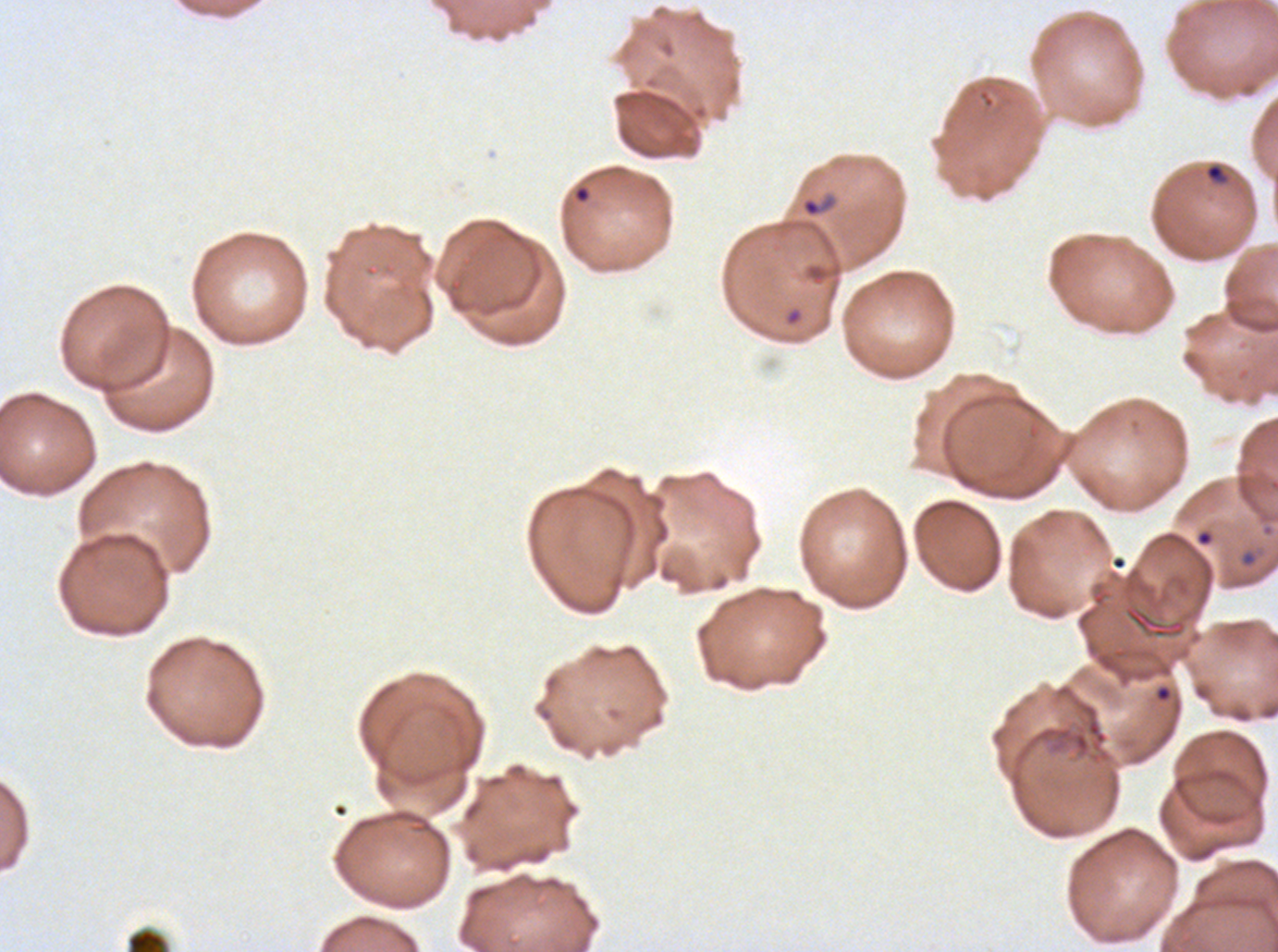

Approximate bounding boxes as [x1, y1, x2, y2] in pixels. Debris locations: [1026, 701, 1111, 764], [126, 927, 169, 951]. Ring locations: [1204, 163, 1228, 185], [572, 184, 592, 204], [800, 191, 839, 219], [1240, 550, 1258, 568], [1154, 684, 1173, 703]. Plasmodium falciparum cultured ex vivo for 24 to 48 hours, from a patient in The Gambia. Thin blood film. Image is 1278×952 pixels. Giemsa-stained preparation. A sub-image separated from a larger composite.